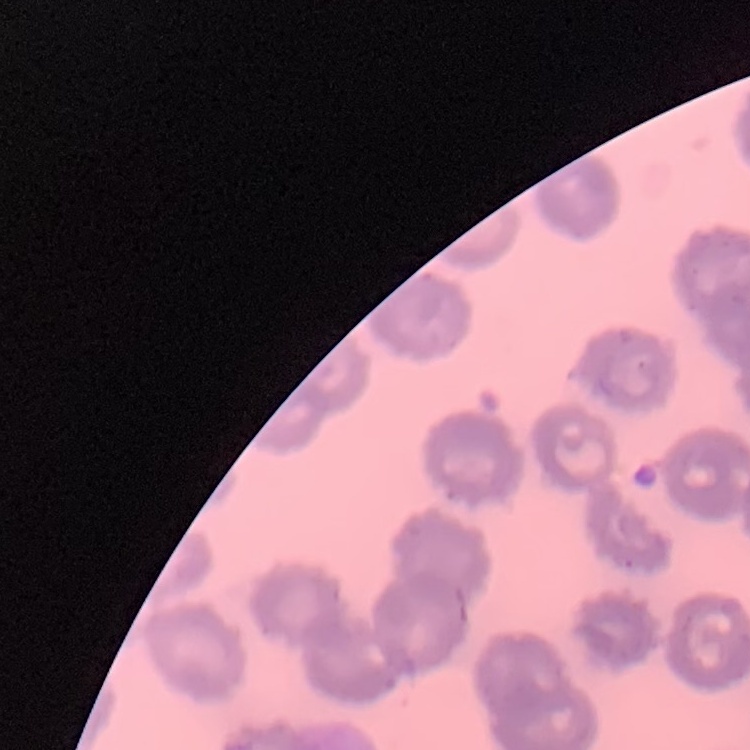

Summary:
  - Erythrocyte morphology: no rouleaux formation
  - Preparation: thin blood smear
  - Stain: Field's or Giemsa
  - Image type: one tile cut from a larger photomicrograph